Name the parasite shown.
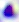

This is Toxoplasma gondii.

Captured at 400x magnification. Photomicrograph.